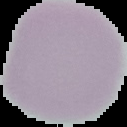

preparation: thin blood smear
malaria_status: uninfected
image_type: cell region segmented out of the field of view; surrounding area masked to black
image_size: 127×127 pixels